Evaluate for Plasmodium parasites.
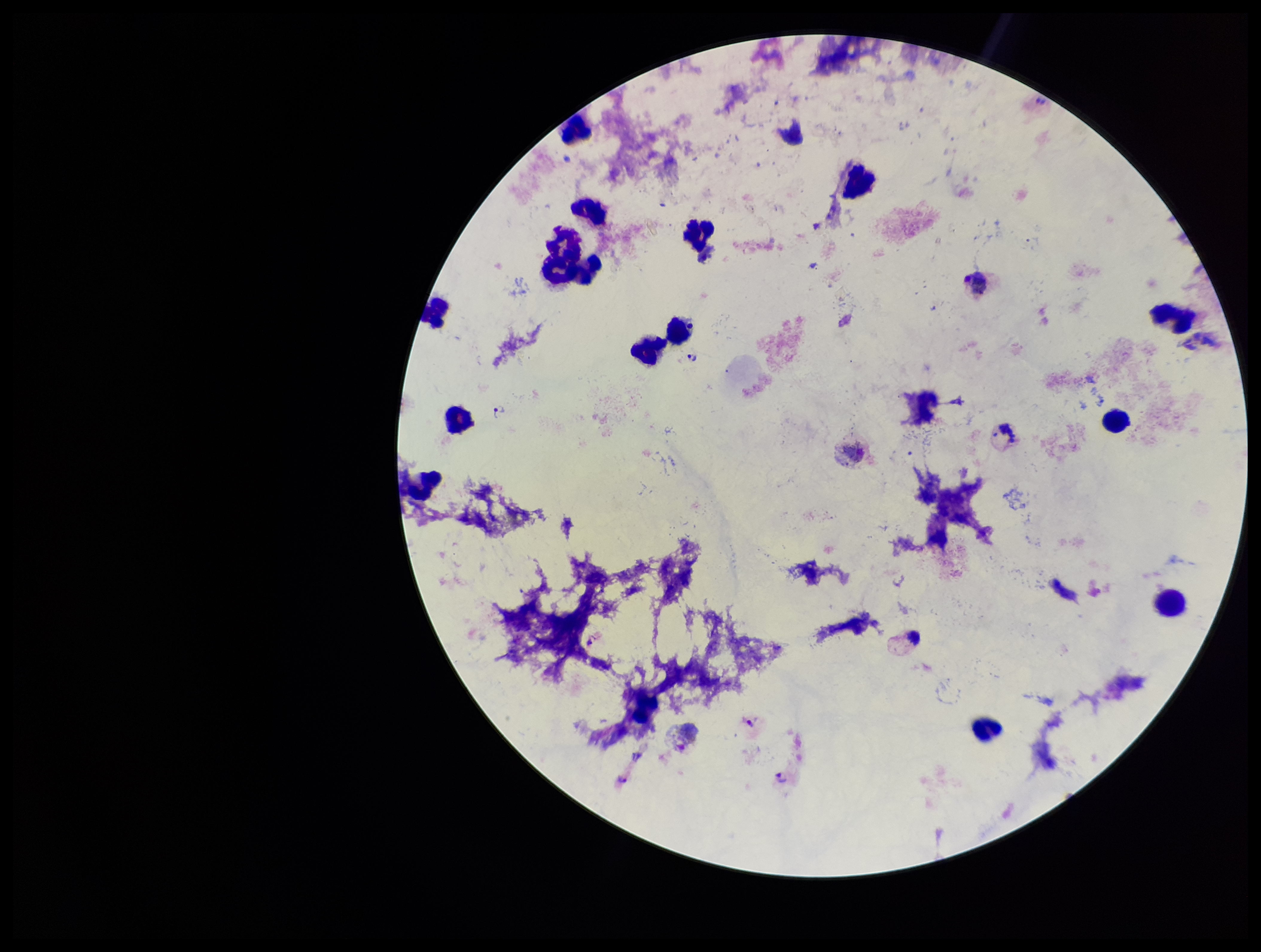
Seen.

capture = smartphone photograph through the microscope eyepiece
field of view = single
parasite count = 6
image size = 1261×952 pixels
leukocyte count = 17
patient malaria status = positive
preparation = thick
species reported for this patient = Plasmodium vivax
stain = Giemsa